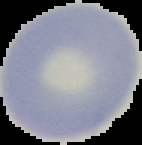

{
  "image_size": "142×145 pixels",
  "result": "negative for malaria parasites",
  "image_type": "segmented cell region on a black background",
  "preparation": "thin blood film"
}